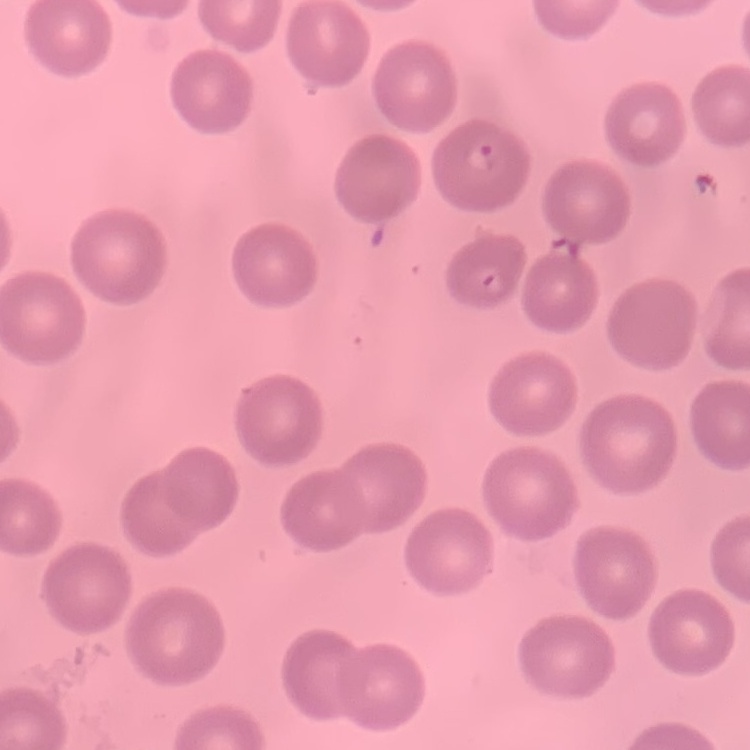

Summary:
  - Red blood cell morphology: no rouleaux formation
  - Image type: one tile cut from a larger photomicrograph
  - Stain: Field's or Giemsa
  - Preparation: thin blood film